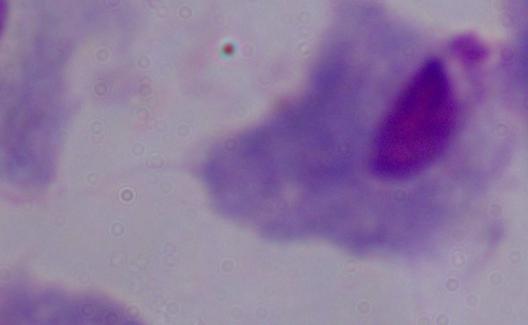

identification = trichomonad
magnification = 1000x
modality = micrograph